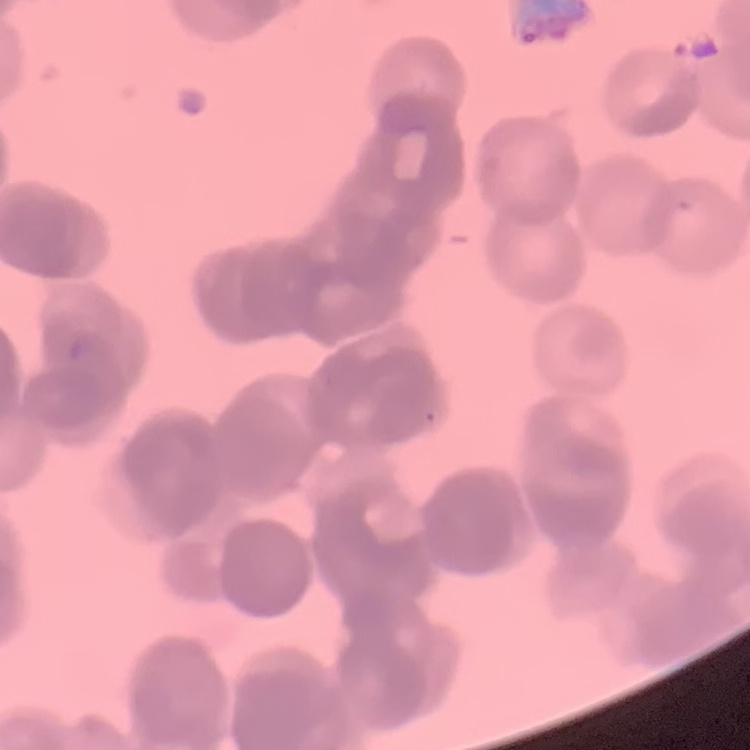
The erythrocytes show rouleaux formation. Square crop of a larger photomicrograph. Field's or Giemsa stain. Thin peripheral smear.